Locate every Plasmodium parasite.
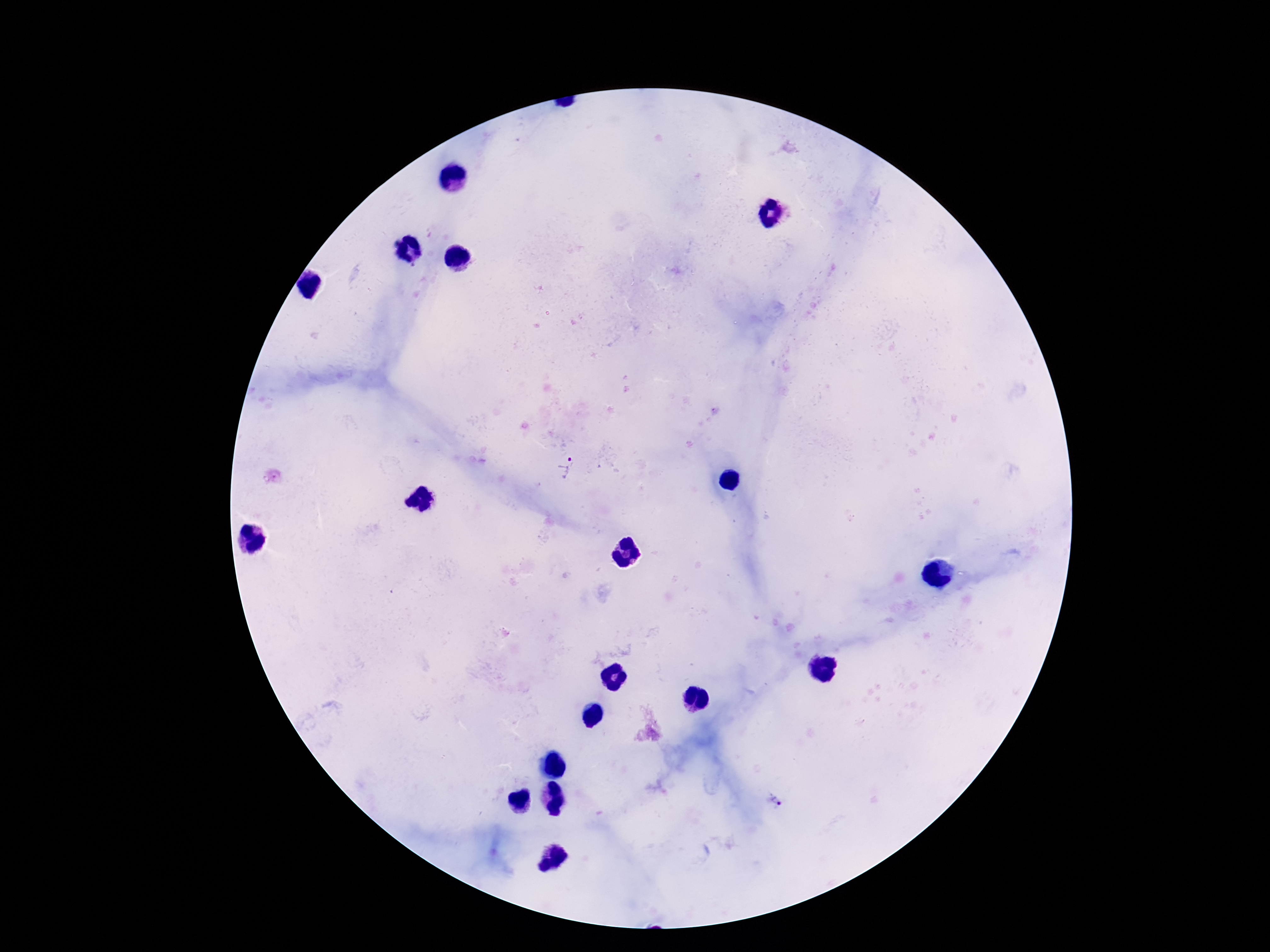
Approximate object centers, in pixels from the top-left corner.
Plasmodium parasites: (x=567, y=467), (x=775, y=804).

Summary:
  - Magnification: 100x
  - Preparation: thick blood film
  - Patient malaria status: positive
  - Stain: Giemsa
  - Capture: smartphone camera through the microscope eyepiece
  - Image size: 1270×952 pixels
  - Field of view: one from this slide